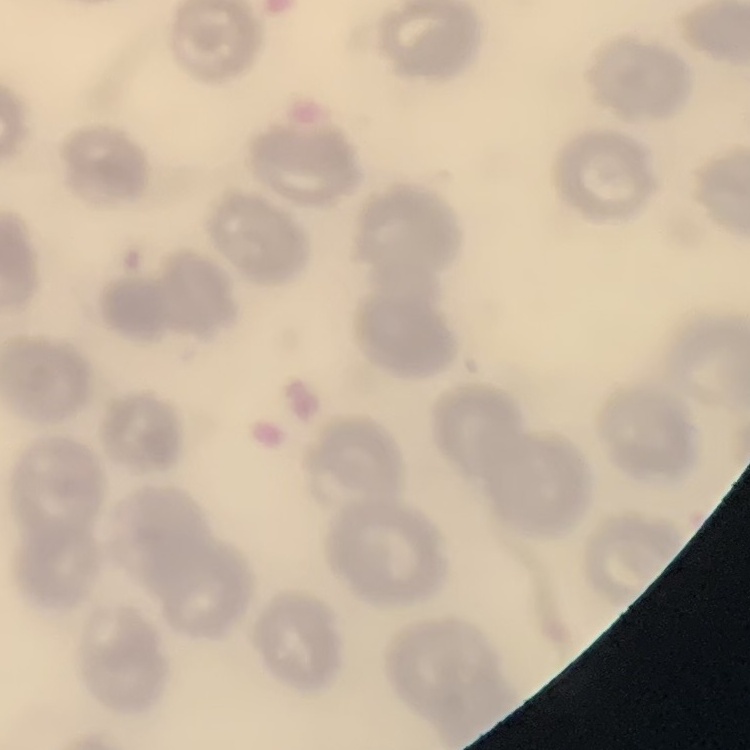
red_blood_cell_morphology: no rouleaux formation
stain: Field's or Giemsa
preparation: thin blood film
image_type: one tile cut from a larger photomicrograph